Report the malaria status of this cell.
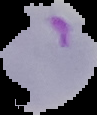
Parasitized.

From a thin blood smear. Image is 97×115 pixels. Segmented cell region on a black background.